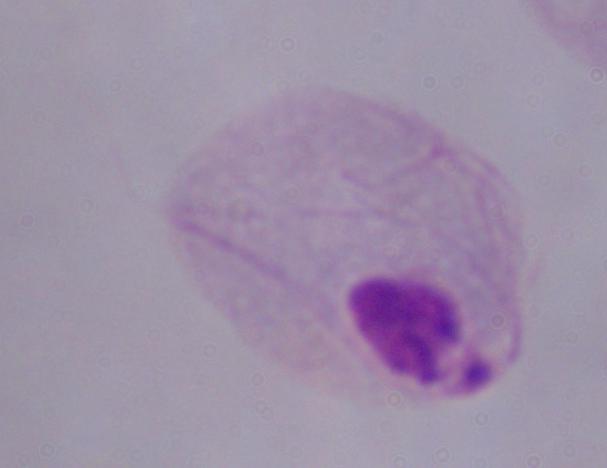
identification = trichomonad
modality = photomicrograph
magnification = 1000x